Classify this cell by malaria status.
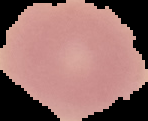

Uninfected.

Summary:
  - Image type: segmented cell region with the area outside set to black
  - Preparation: thin blood film
  - Image size: 148×121 pixels